Assess this cell for malaria.
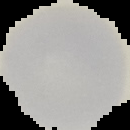

Uninfected.

Summary:
  - Image size: 130×130 pixels
  - Image type: segmented cell region on a black background
  - Preparation: thin blood film